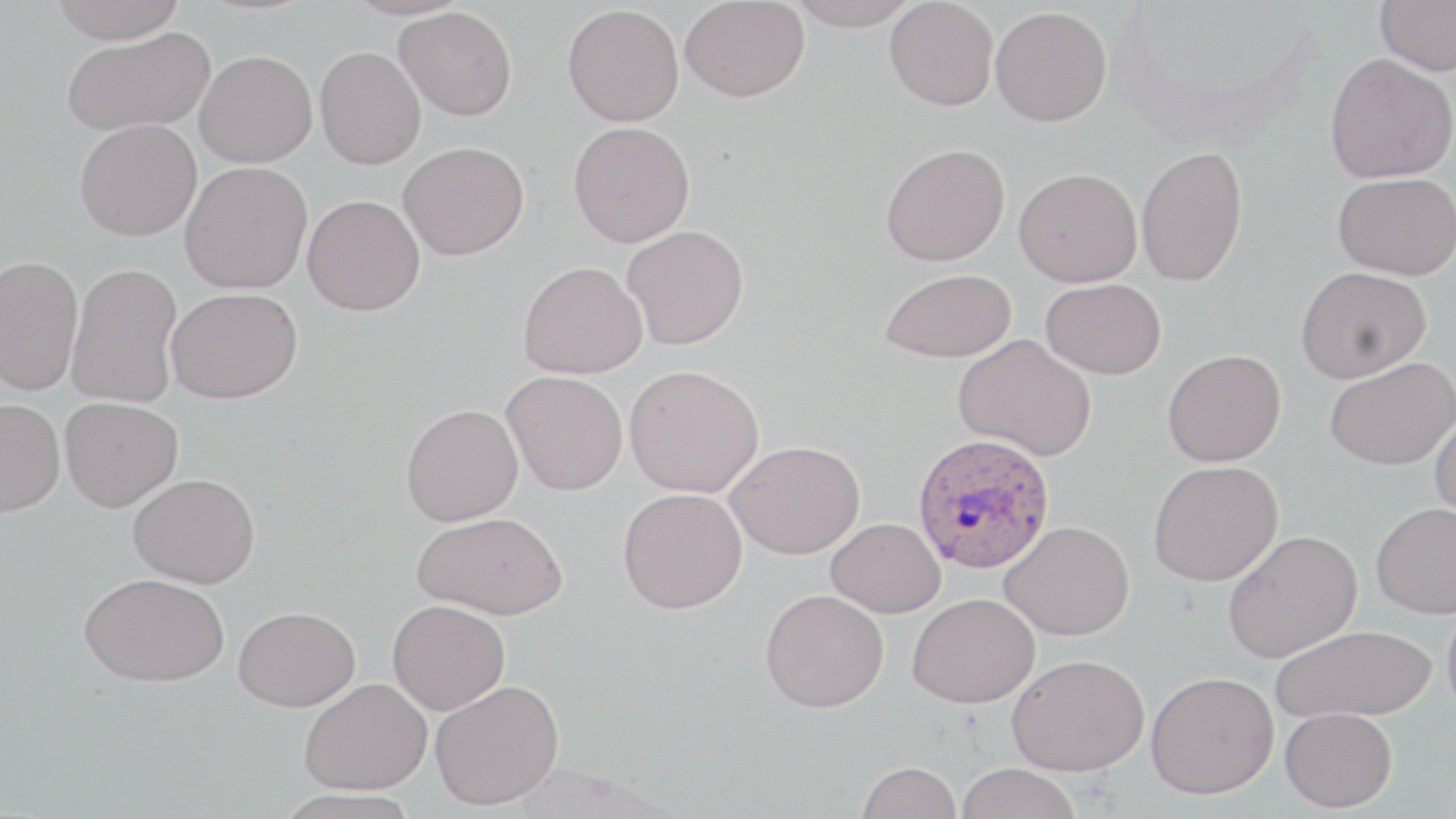
{
  "plasmodium_ovale_infected_red_blood_cell_locations": "approximate bounding boxes as [x1, y1, x2, y2] in pixels: [912, 432, 1056, 575]",
  "slide_level_diagnosis": "Plasmodium ovale",
  "uninfected_red_blood_cell_locations": "approximate bounding boxes as [x1, y1, x2, y2] in pixels: [47, 0, 190, 43], [341, 0, 474, 20], [680, 0, 810, 102], [787, 0, 920, 30], [885, 0, 999, 111], [1375, 0, 1456, 76], [563, 4, 684, 127], [394, 6, 517, 120], [990, 6, 1111, 126], [61, 27, 214, 136], [315, 45, 426, 169], [194, 50, 317, 168], [1324, 53, 1456, 183], [75, 118, 202, 241], [568, 121, 695, 247], [397, 141, 530, 260], [880, 142, 1010, 266], [1135, 145, 1248, 287], [179, 161, 313, 294], [1014, 167, 1142, 287], [1332, 171, 1456, 280], [302, 194, 425, 315], [621, 225, 749, 350], [0, 254, 84, 396], [518, 260, 648, 378], [67, 262, 183, 408], [1296, 265, 1431, 383], [880, 268, 1016, 363], [1041, 278, 1167, 379], [166, 286, 303, 403], [953, 333, 1097, 461], [1162, 349, 1286, 467], [1324, 357, 1456, 470], [624, 363, 764, 498], [502, 370, 628, 495], [59, 396, 183, 511], [0, 397, 65, 517], [401, 403, 523, 525], [1429, 410, 1456, 527], [725, 439, 865, 559], [1148, 460, 1283, 586], [127, 472, 261, 588], [618, 487, 748, 614], [1370, 501, 1456, 619], [412, 511, 568, 619], [825, 517, 946, 618], [998, 521, 1136, 640], [1222, 529, 1363, 663], [79, 571, 231, 686], [760, 589, 889, 713], [907, 592, 1041, 709], [1442, 597, 1456, 723], [388, 599, 510, 714], [233, 606, 360, 711], [1270, 624, 1437, 723], [1007, 653, 1149, 775], [1146, 671, 1279, 799], [300, 678, 432, 794], [430, 679, 564, 809], [1280, 706, 1397, 812], [856, 760, 963, 819], [957, 763, 1081, 819], [274, 788, 425, 819]",
  "field_of_view": "one of a larger specimen",
  "stain": "May-Grünwald-Giemsa",
  "preparation": "thin blood smear",
  "image_size": "1456×819 pixels",
  "magnification": "1000x",
  "modality": "light microscopy"
}